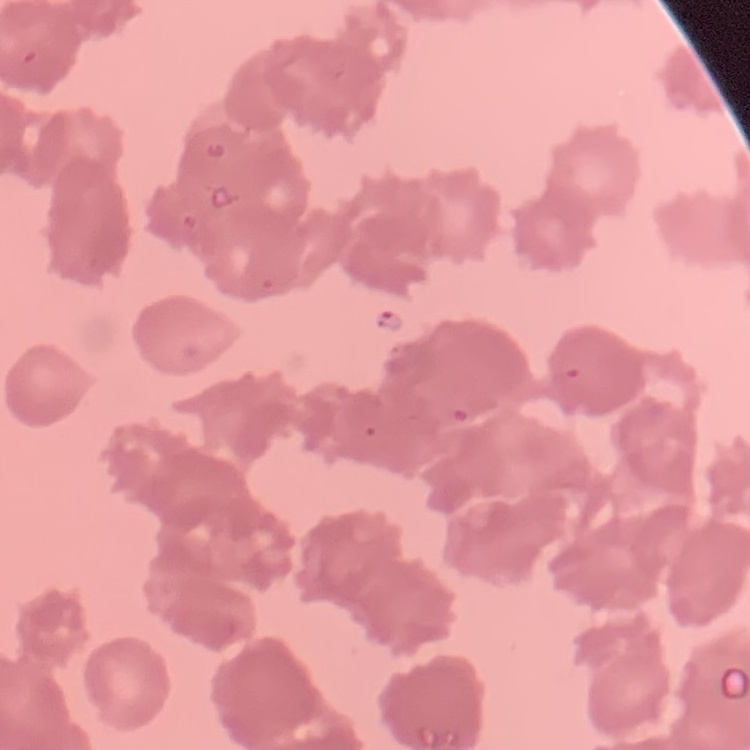

Summary:
  - Red blood cell morphology: rouleaux formation
  - Image type: square crop of a larger photomicrograph
  - Preparation: thin blood smear
  - Stain: Field's or Giemsa